Assess this cell for malaria.
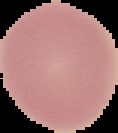

It is uninfected.

Segmented cell region on a black background. From a thin blood smear. Image is 118×133 pixels.